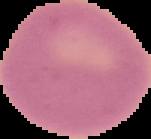 Malaria status: uninfected. From a thin blood film. Image is 151×139 pixels. Cell region segmented out of the field of view; the surrounding area is masked to black.